Report the malaria status of this cell.
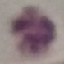
Uninfected.

Acquired by smartphone through the microscope eyepiece. Giemsa-stained preparation. Cell patch, automatically extracted from a larger field of view and resized to 64 × 64 pixels. Thin blood film.